Classify this cell by malaria status.
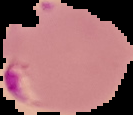
Parasitized.

{
  "preparation": "thin blood film",
  "image_size": "133×115 pixels",
  "image_type": "cell region segmented out of the field of view; surrounding area masked to black"
}